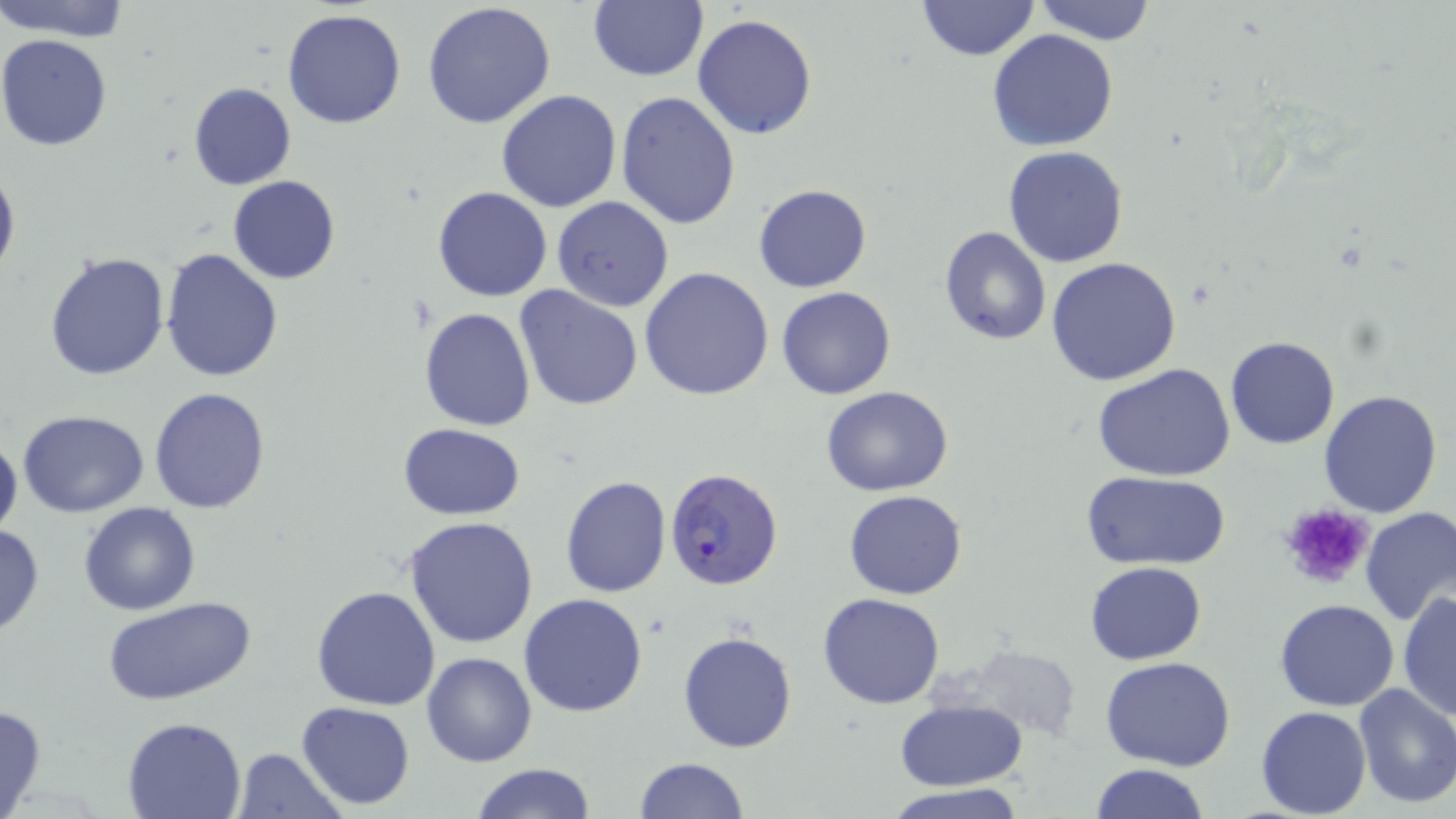

{
  "slide_level_diagnosis": "Plasmodium falciparum",
  "preparation": "thin blood film",
  "modality": "light microscopy",
  "uninfected_red_blood_cell_locations": "approximate bounding boxes as (x1, y1, x2, y2) in pixels: (2, 0, 134, 41), (588, 0, 708, 82), (916, 0, 1039, 62), (1034, 0, 1156, 44), (421, 1, 557, 129), (283, 8, 408, 130), (693, 14, 817, 140), (987, 30, 1120, 152), (1, 33, 116, 151), (188, 82, 295, 191), (495, 89, 622, 212), (615, 91, 741, 230), (1004, 146, 1129, 266), (0, 160, 20, 285), (228, 176, 340, 285), (753, 182, 873, 293), (432, 185, 553, 303), (551, 197, 674, 312), (938, 227, 1053, 346), (159, 248, 284, 382), (42, 249, 171, 380), (1046, 257, 1181, 386), (640, 267, 774, 400), (513, 286, 643, 410), (776, 286, 897, 400), (419, 306, 536, 431), (1226, 336, 1339, 449), (1093, 365, 1238, 482), (821, 386, 953, 496), (149, 387, 271, 514), (1317, 388, 1443, 518), (17, 410, 150, 517), (398, 423, 526, 521), (0, 429, 22, 542), (1080, 471, 1231, 570), (559, 475, 670, 597), (843, 490, 967, 600), (80, 502, 201, 617), (1358, 506, 1456, 627), (404, 517, 540, 649), (0, 523, 45, 637), (1085, 561, 1207, 666), (312, 586, 441, 710), (1397, 591, 1455, 721), (519, 593, 649, 718), (818, 593, 946, 710), (104, 596, 257, 707), (1275, 599, 1400, 712), (678, 631, 797, 753), (952, 644, 1085, 743), (421, 651, 537, 767), (1101, 657, 1236, 772), (1352, 682, 1456, 808), (896, 700, 1027, 791), (296, 701, 415, 810), (0, 703, 47, 818), (1256, 706, 1371, 818), (121, 716, 247, 819), (232, 748, 346, 818), (634, 757, 749, 818), (470, 762, 597, 819), (1087, 764, 1209, 819), (882, 786, 1030, 818)",
  "plasmodium_falciparum_infected_red_blood_cell_locations": "approximate bounding boxes as (x1, y1, x2, y2) in pixels: (665, 471, 785, 592)",
  "stain": "May-Grünwald-Giemsa",
  "field_of_view": "single",
  "magnification": "1000x",
  "platelet_locations": "approximate bounding boxes as (x1, y1, x2, y2) in pixels: (1278, 503, 1374, 590)",
  "image_size": "1456×819 pixels"
}